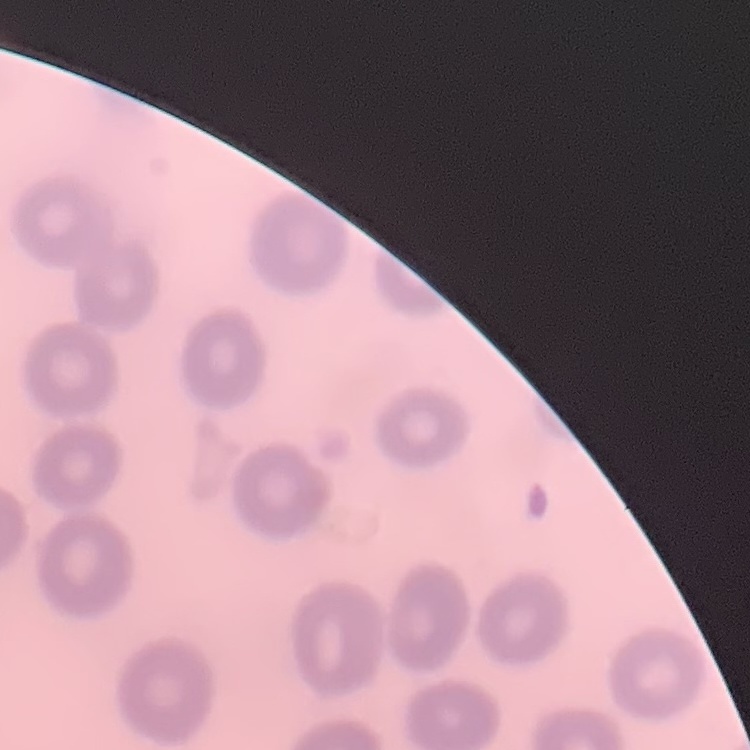
Summary:
  - Red blood cell morphology: no rouleaux formation
  - Preparation: thin peripheral smear
  - Stain: Field's or Giemsa
  - Image type: one tile cut from a larger photomicrograph